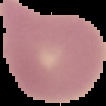 Result: no malaria parasites detected. From a thin blood film. Cell region segmented out of the field of view; the surrounding area is masked to black. Image is 106×106 pixels.